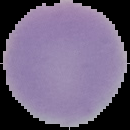
From a thin blood film. Image is 130×130 pixels. Segmented cell region on a black background. Malaria status: uninfected.